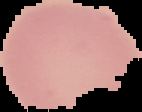
preparation: thin blood smear
image_size: 142×112 pixels
image_type: segmented cell region on a black background
result: no malaria parasites detected